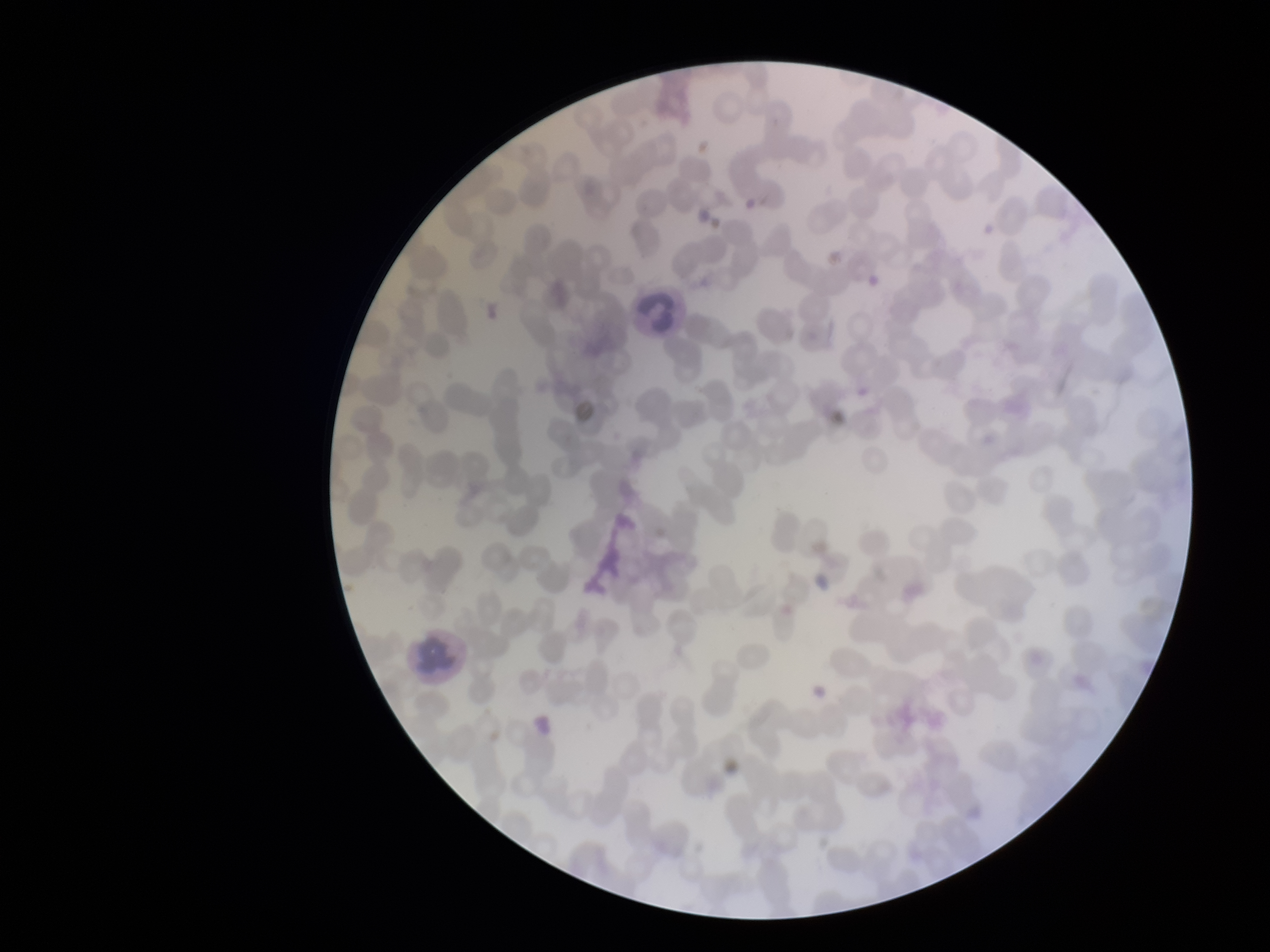

Summary:
  - Stain: Giemsa
  - Patient malaria status: negative
  - Preparation: thin smear
  - Parasitized red blood cell count: 0
  - Red blood cell count: 259
  - Field of view: single
  - Parasitized red blood cells: none detected
  - Capture: smartphone photograph through the microscope eyepiece
  - Image size: 1270×952 pixels